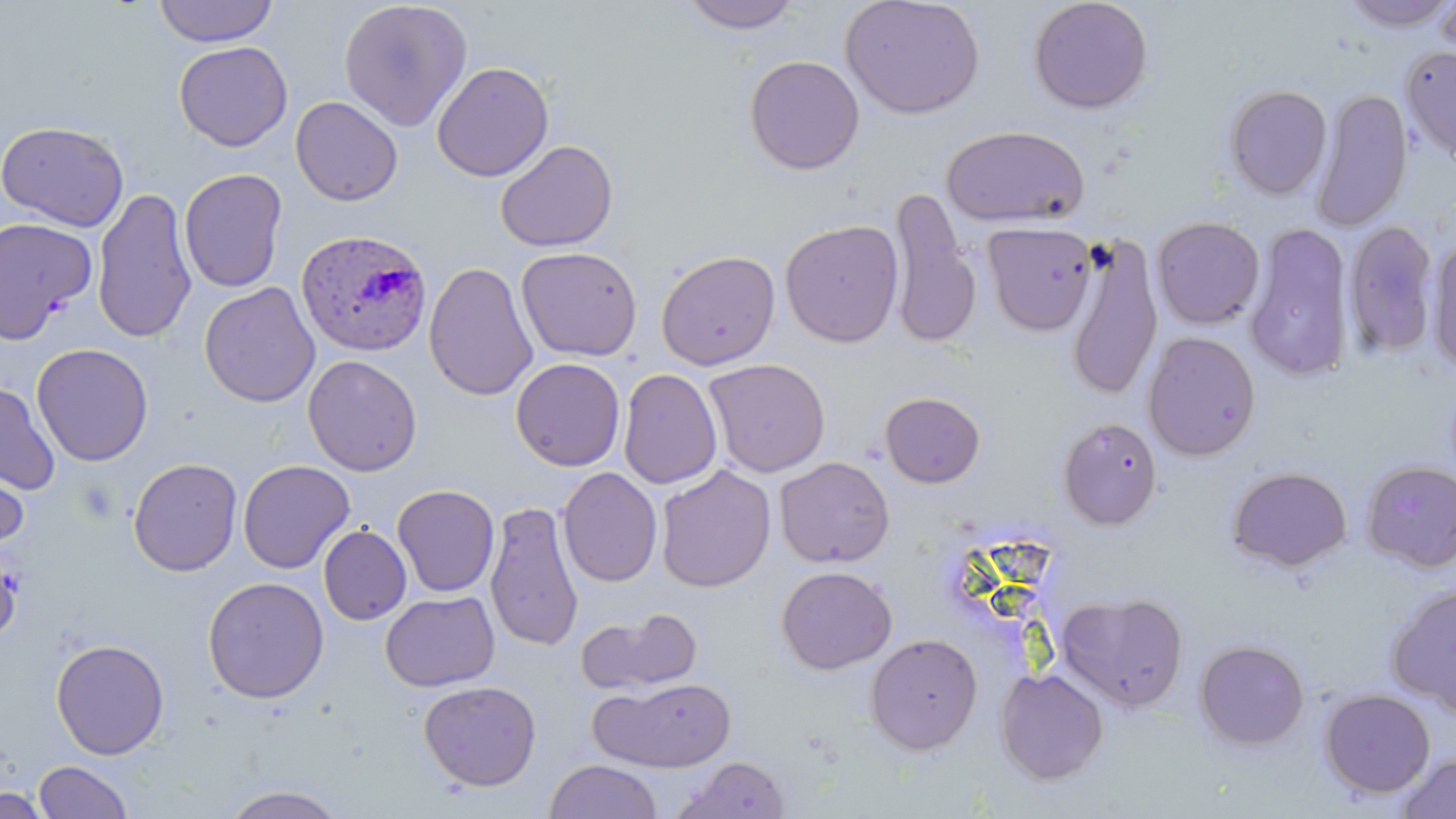
slide-level diagnosis = Plasmodium ovale
modality = light microscopy
preparation = thin blood smear
stain = May-Grünwald-Giemsa
uninfected red blood cell locations = approximate bounding boxes as named x1/y1/x2/y2 corners in pixels: (x1=153, y1=0, x2=279, y2=47), (x1=338, y1=0, x2=473, y2=131), (x1=677, y1=0, x2=804, y2=34), (x1=839, y1=0, x2=986, y2=120), (x1=1028, y1=0, x2=1154, y2=114), (x1=1338, y1=0, x2=1456, y2=31), (x1=1435, y1=2, x2=1456, y2=59), (x1=173, y1=41, x2=293, y2=151), (x1=1400, y1=45, x2=1456, y2=163), (x1=743, y1=55, x2=865, y2=175), (x1=432, y1=61, x2=554, y2=182), (x1=1223, y1=83, x2=1332, y2=200), (x1=1311, y1=88, x2=1413, y2=232), (x1=290, y1=95, x2=403, y2=206), (x1=0, y1=120, x2=130, y2=232), (x1=941, y1=124, x2=1090, y2=228), (x1=495, y1=139, x2=619, y2=253), (x1=178, y1=168, x2=288, y2=293), (x1=91, y1=187, x2=197, y2=343), (x1=889, y1=190, x2=981, y2=348), (x1=0, y1=216, x2=97, y2=344), (x1=1152, y1=216, x2=1265, y2=329), (x1=779, y1=219, x2=904, y2=348), (x1=1344, y1=219, x2=1439, y2=360), (x1=982, y1=221, x2=1098, y2=336), (x1=1244, y1=223, x2=1355, y2=381), (x1=1065, y1=233, x2=1164, y2=402), (x1=1426, y1=237, x2=1456, y2=375), (x1=515, y1=246, x2=643, y2=361), (x1=655, y1=249, x2=780, y2=370), (x1=424, y1=261, x2=538, y2=401), (x1=199, y1=282, x2=320, y2=408), (x1=1142, y1=331, x2=1261, y2=461), (x1=31, y1=343, x2=154, y2=466), (x1=302, y1=354, x2=422, y2=476), (x1=510, y1=357, x2=626, y2=472), (x1=702, y1=358, x2=831, y2=478), (x1=618, y1=368, x2=723, y2=490), (x1=0, y1=382, x2=61, y2=496), (x1=879, y1=391, x2=986, y2=488), (x1=1057, y1=416, x2=1162, y2=529), (x1=0, y1=452, x2=30, y2=553), (x1=774, y1=456, x2=895, y2=568), (x1=127, y1=457, x2=243, y2=576), (x1=237, y1=459, x2=354, y2=574), (x1=1361, y1=460, x2=1456, y2=572), (x1=654, y1=465, x2=776, y2=593), (x1=1227, y1=466, x2=1352, y2=572), (x1=557, y1=467, x2=662, y2=587), (x1=392, y1=484, x2=500, y2=596), (x1=485, y1=500, x2=584, y2=651), (x1=318, y1=525, x2=412, y2=625), (x1=0, y1=540, x2=22, y2=646), (x1=775, y1=565, x2=897, y2=675), (x1=202, y1=576, x2=330, y2=704), (x1=1386, y1=584, x2=1456, y2=718), (x1=1056, y1=590, x2=1189, y2=711), (x1=380, y1=591, x2=500, y2=692), (x1=576, y1=606, x2=704, y2=697), (x1=866, y1=633, x2=983, y2=754), (x1=51, y1=638, x2=170, y2=760), (x1=1194, y1=639, x2=1310, y2=750), (x1=995, y1=668, x2=1108, y2=784), (x1=591, y1=677, x2=737, y2=772), (x1=418, y1=680, x2=542, y2=792), (x1=1319, y1=689, x2=1436, y2=798), (x1=1395, y1=753, x2=1456, y2=818), (x1=673, y1=756, x2=792, y2=818), (x1=544, y1=758, x2=663, y2=818), (x1=33, y1=760, x2=134, y2=818), (x1=221, y1=784, x2=349, y2=818), (x1=0, y1=785, x2=54, y2=817)
magnification = 1000x
field of view = single
Plasmodium ovale-infected red blood cell locations = approximate bounding boxes as named x1/y1/x2/y2 corners in pixels: (x1=296, y1=227, x2=433, y2=357)
image size = 1456×819 pixels